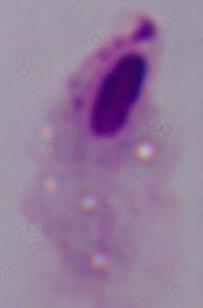
identification: trichomonad
magnification: 1000x
modality: micrograph